Identify the preparation type.
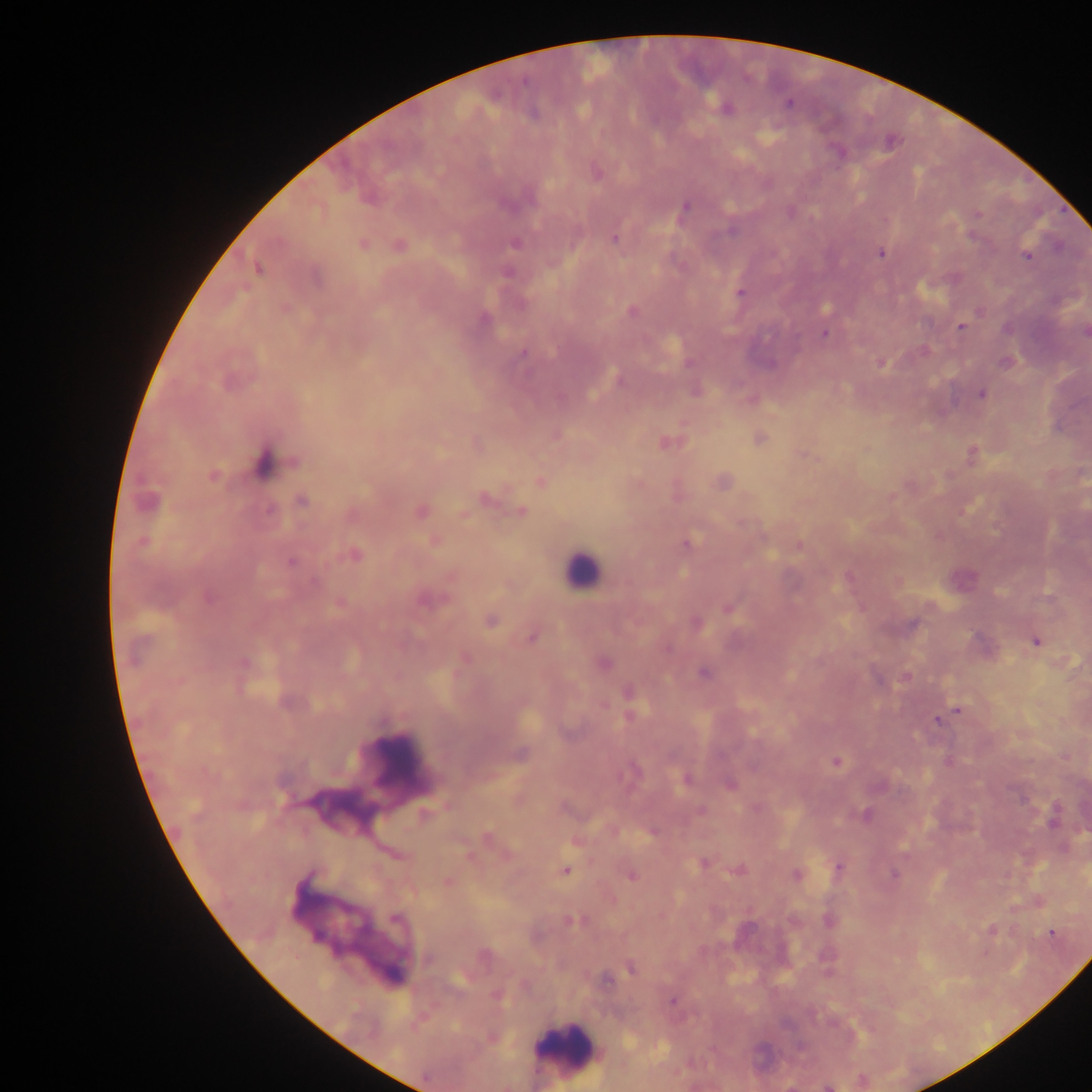

Thick blood film.

Approximate centers as (x, y) in pixels.
Summary:
  - Leukocyte locations: (580, 571), (401, 759), (566, 1047)
  - Plasmodium parasite locations: (788, 103), (726, 109), (596, 172), (684, 208), (732, 231), (973, 238), (614, 240), (515, 243), (363, 245), (398, 246), (881, 254), (1026, 255), (258, 269), (740, 293), (631, 311), (484, 319), (960, 327), (1085, 333), (824, 334), (522, 354), (1005, 362), (688, 363), (881, 363), (770, 364), (620, 380), (981, 394), (761, 439), (666, 442), (972, 454), (263, 462), (213, 476), (541, 482), (722, 483), (484, 499), (147, 501), (302, 501), (269, 510), (421, 511), (521, 512), (435, 541), (143, 542), (687, 544), (799, 545), (355, 555), (291, 562), (848, 577), (315, 583), (209, 599), (425, 600), (340, 603), (729, 608), (491, 621), (696, 623), (913, 625), (531, 638), (1035, 642), (667, 649), (244, 663), (603, 663), (704, 673), (905, 676), (628, 692), (287, 703), (958, 711), (630, 716), (937, 721), (520, 754), (836, 762), (632, 770), (686, 779), (730, 784), (1022, 799), (701, 811), (426, 814), (865, 815), (1054, 822), (652, 833), (488, 838), (469, 856), (704, 863), (838, 867), (738, 870), (565, 871), (895, 874), (796, 875), (631, 876), (447, 881), (395, 919), (829, 921), (572, 922), (992, 930), (1052, 933), (483, 955), (428, 960), (631, 969), (605, 980), (497, 997), (672, 1002), (861, 1080), (828, 1087)
  - Capture: mobile-phone photograph through a microscope
  - Image size: 1092×1092 pixels
  - Country: Ghana
  - Field of view: single